Classify this cell by malaria status.
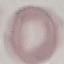
Uninfected.

preparation = thin smear
stain = Giemsa
capture = smartphone camera at the microscope eyepiece
image type = automatically extracted cell patch, resized to 64 × 64 pixels